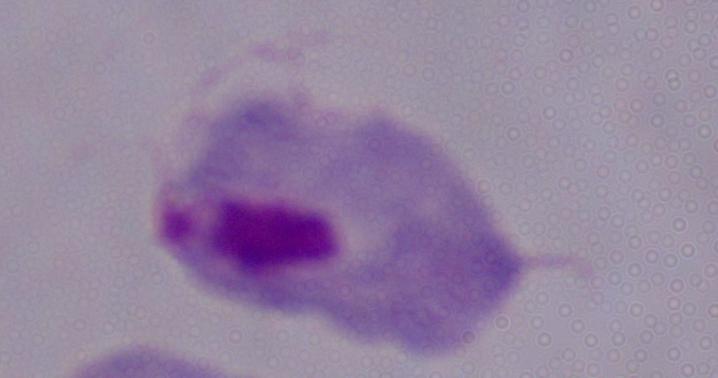 A trichomonad is seen. 1000x magnification. Photomicrograph.